Comment on the morphology of the erythrocytes.
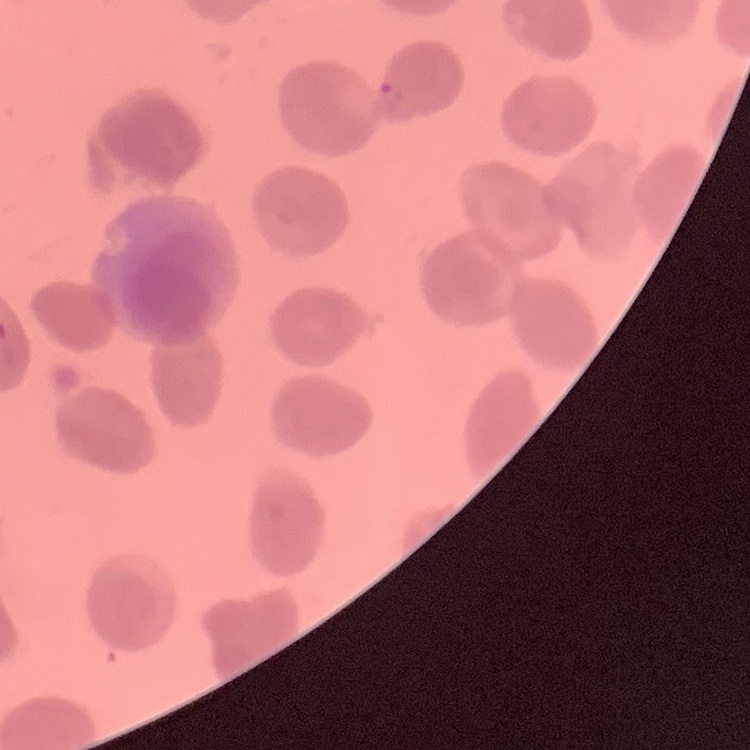

No rouleaux formation.

preparation = thin peripheral smear
stain = Field's or Giemsa
image type = one tile cut from a larger photomicrograph